Locate and identify every blood parasite.
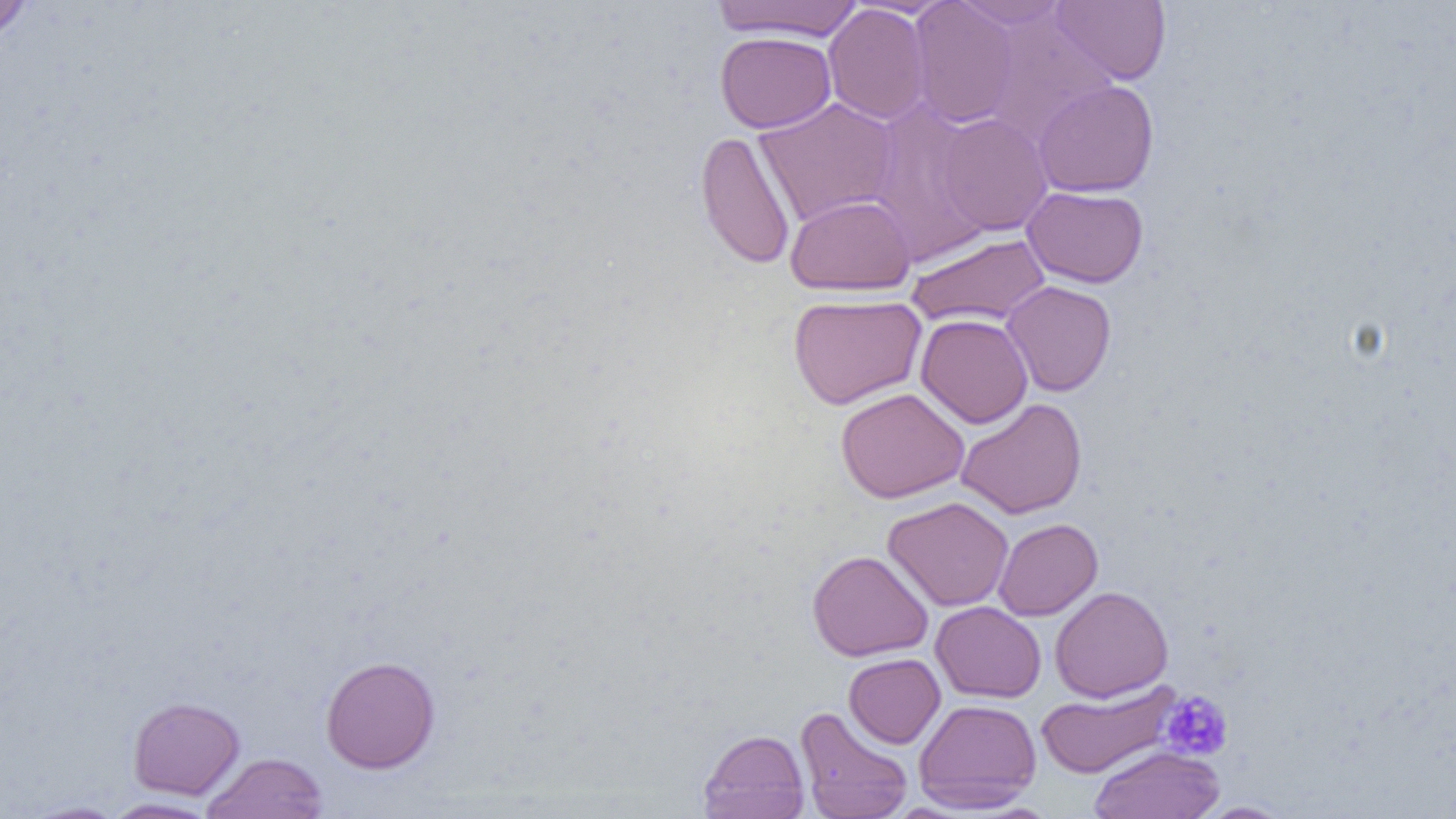

No blood parasites seen.

Approximate bounding boxes as (x1,y1)-(x2,y2) corner pairs in pixels. Uninfected red blood cell locations: (0,0)-(39,44), (908,0)-(1020,128), (951,0)-(1071,29), (1051,0)-(1171,85), (712,1)-(864,41), (823,3)-(931,125), (982,12)-(1119,145), (715,31)-(836,133), (1032,79)-(1159,197), (754,97)-(899,228), (866,102)-(994,266), (936,112)-(1053,235), (695,130)-(796,270), (1022,186)-(1148,288), (785,194)-(915,296), (906,233)-(1051,328), (1001,280)-(1116,397), (787,293)-(927,410), (916,314)-(1033,428), (835,387)-(970,503), (956,397)-(1087,519), (882,496)-(1014,612), (993,518)-(1103,620), (807,550)-(933,661), (1050,586)-(1173,702), (930,601)-(1046,703), (843,653)-(946,748), (320,655)-(440,773), (1035,680)-(1181,779), (128,696)-(245,799), (913,698)-(1042,812), (816,705)-(1015,816), (795,706)-(914,819), (697,729)-(810,819), (1089,744)-(1225,818), (202,752)-(328,819), (100,797)-(221,818), (20,800)-(128,818), (1193,801)-(1298,818). Platelet locations: (1160,690)-(1234,761). Slide-level diagnosis: negative for blood parasites. Image is 1456×819 pixels. Captured at 1000x magnification. Thin blood film. Light microscopy. One field of a larger specimen.